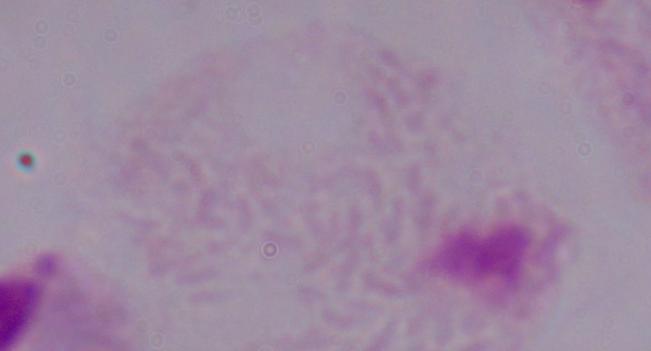 A trichomonad is shown. Captured at 1000x magnification. Photomicrograph.